Comment on the morphology of the erythrocytes.
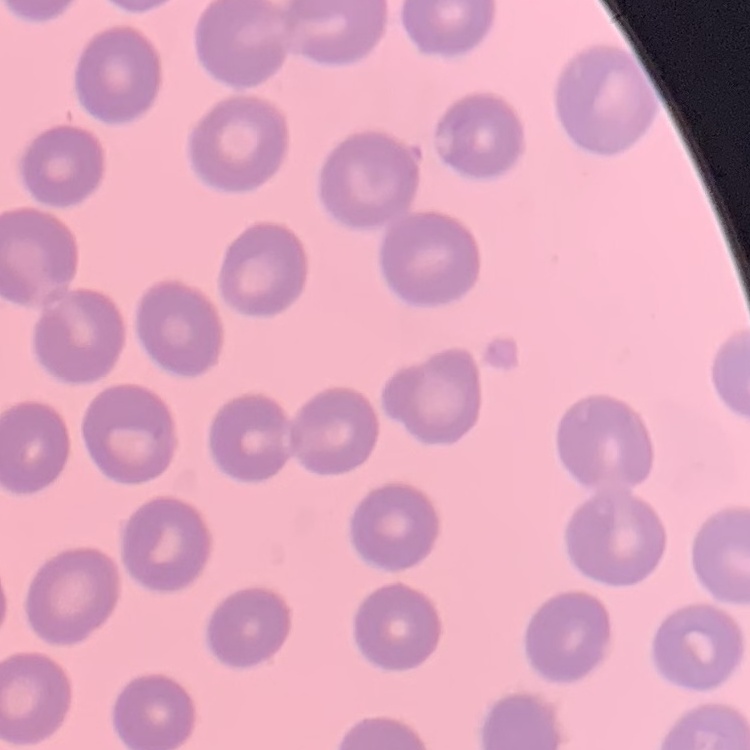

No rouleaux formation.

Summary:
  - Image type: square crop of a larger photomicrograph
  - Stain: Field's or Giemsa
  - Preparation: thin peripheral smear